Locate and identify every blood parasite.
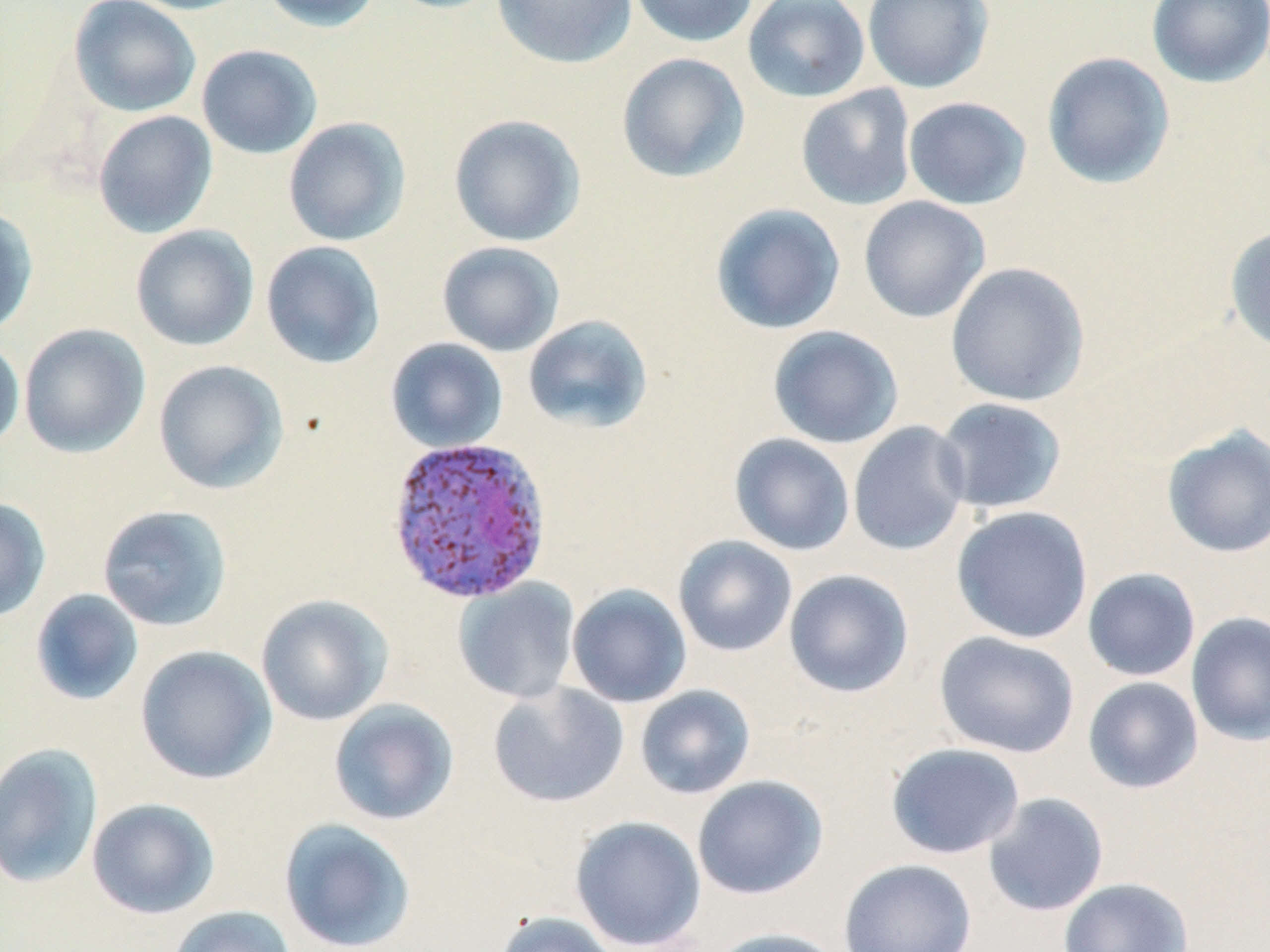
Approximate bounding boxes as (x1,y1)-(x2,y2) corner pairs in pixels.
Plasmodium vivax-infected red blood cells: (385,435)-(554,606).
No Plasmodium falciparum, Plasmodium ovale, Plasmodium malariae, Babesia divergens, or Trypanosoma brucei observed.

{
  "slide_level_diagnosis": "Plasmodium vivax",
  "preparation": "thin blood smear",
  "image_size": "1270×952 pixels",
  "magnification": "1000x",
  "modality": "light microscopy",
  "stain": "May-Grünwald-Giemsa",
  "uninfected_red_blood_cell_locations": "approximate bounding boxes as (x1,y1)-(x2,y2) corner pairs in pixels: (68,0)-(201,118), (121,0)-(255,15), (259,0)-(384,33), (381,0)-(508,14), (492,0)-(638,69), (627,0)-(760,47), (742,0)-(871,103), (862,0)-(994,93), (1147,0)-(1270,87), (196,44)-(323,159), (1041,51)-(1176,189), (616,52)-(751,183), (795,84)-(917,211), (903,96)-(1032,210), (92,110)-(218,239), (448,113)-(586,247), (283,117)-(412,246), (858,196)-(991,323), (710,203)-(846,335), (0,204)-(38,338), (130,224)-(259,351), (1224,225)-(1270,355), (261,241)-(385,369), (436,241)-(566,357), (945,262)-(1090,407), (522,314)-(654,434), (18,323)-(151,458), (767,325)-(904,448), (0,337)-(25,454), (385,337)-(508,453), (153,359)-(289,494), (933,397)-(1068,515), (847,421)-(972,556), (1161,426)-(1270,558), (729,433)-(855,556), (0,496)-(51,623), (96,504)-(233,632), (951,505)-(1093,644), (673,535)-(798,657), (1082,567)-(1201,682), (784,569)-(915,699), (453,578)-(581,704), (567,583)-(692,708), (30,589)-(144,706), (255,593)-(394,726), (1186,611)-(1270,746), (933,631)-(1080,758), (135,645)-(277,784), (1082,677)-(1204,794), (487,682)-(630,808), (635,685)-(756,799), (328,698)-(460,826), (0,742)-(103,889), (886,743)-(1025,859), (692,775)-(828,900), (981,792)-(1109,917), (86,797)-(220,919), (569,815)-(706,951), (278,817)-(417,952), (837,858)-(977,952), (1058,877)-(1192,952), (167,905)-(297,952), (491,911)-(623,952), (706,927)-(846,952)",
  "field_of_view": "one of a larger specimen"
}